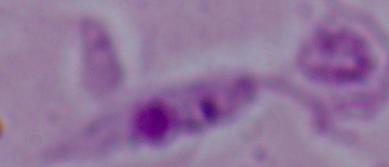
{
  "modality": "micrograph",
  "magnification": "1000x",
  "identification": "Leishmania"
}